Outline each blood parasite and name the species.
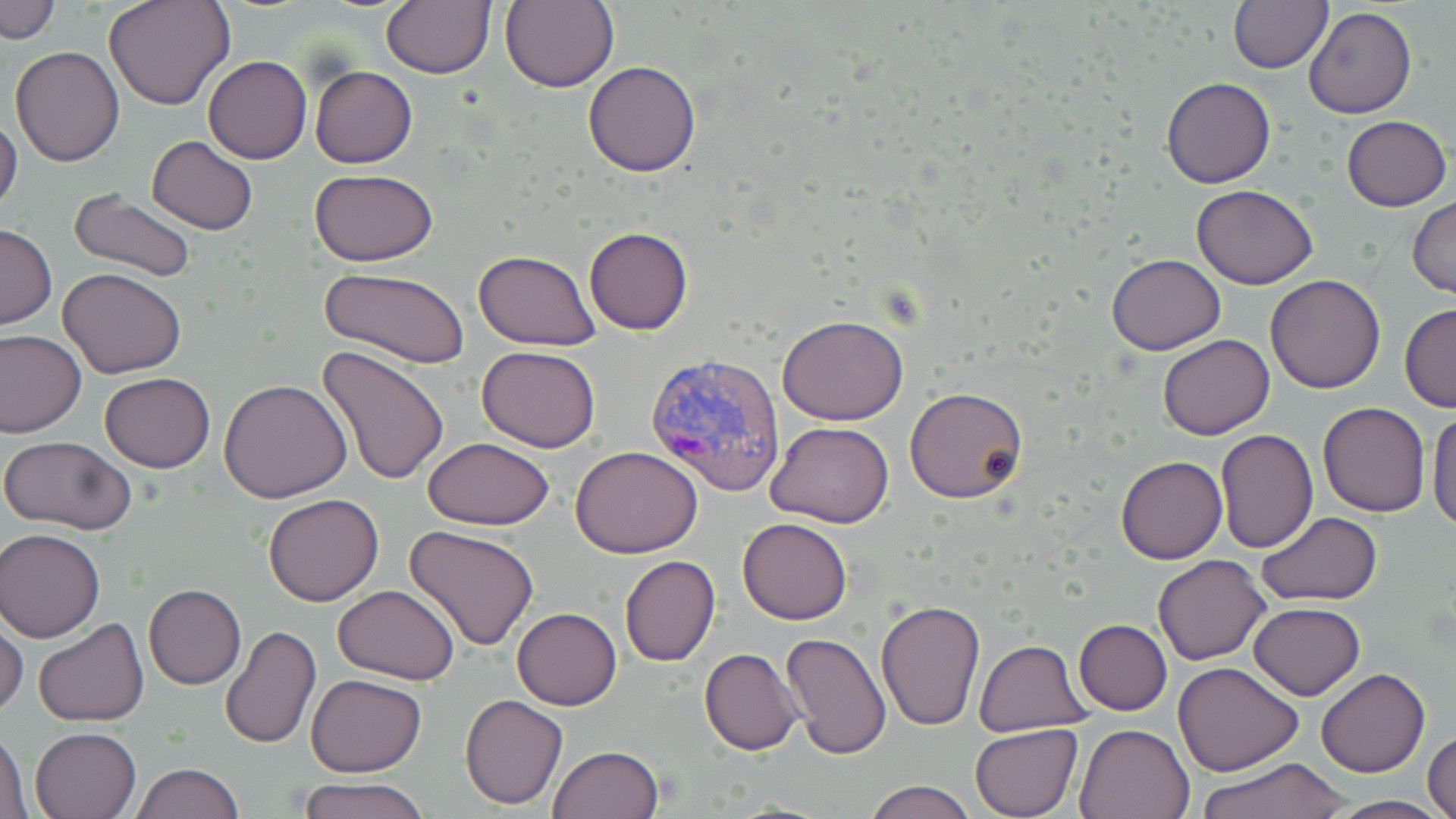

Approximate bounding boxes as (x1,y1)-(x2,y2) corner pairs in pixels.
Plasmodium vivax-infected red blood cells: (642,351)-(788,497).
No Plasmodium falciparum, Plasmodium ovale, Plasmodium malariae, Babesia divergens, or Trypanosoma brucei observed.

Uninfected red blood cell locations: (2,0)-(62,44), (103,0)-(235,111), (381,0)-(495,79), (1228,0)-(1334,74), (499,1)-(618,93), (1302,7)-(1417,118), (10,46)-(126,166), (204,57)-(312,164), (583,61)-(700,176), (309,65)-(417,167), (1159,76)-(1276,188), (1340,114)-(1451,211), (0,115)-(22,220), (147,136)-(260,235), (309,169)-(438,267), (1192,185)-(1319,289), (67,188)-(198,283), (1409,197)-(1456,297), (0,223)-(57,329), (584,226)-(693,336), (472,249)-(598,348), (1105,254)-(1228,355), (58,267)-(187,380), (320,267)-(471,369), (1265,274)-(1386,394), (1399,304)-(1456,413), (778,315)-(908,423), (0,329)-(85,438), (1156,334)-(1275,439), (316,345)-(448,485), (476,345)-(601,452), (99,372)-(216,472), (219,379)-(351,503), (904,388)-(1028,503), (1318,401)-(1430,518), (1427,407)-(1456,531), (765,421)-(894,529), (1214,429)-(1317,552), (0,436)-(136,533), (424,436)-(554,529), (571,445)-(703,559), (1116,455)-(1227,564), (262,494)-(383,607), (1258,512)-(1383,605), (738,517)-(853,625), (405,523)-(541,650), (1,529)-(105,642), (1152,554)-(1271,665), (619,555)-(720,667), (144,584)-(246,689), (332,584)-(460,683), (876,599)-(986,731), (1247,601)-(1365,700), (512,608)-(622,710), (0,615)-(28,717), (32,617)-(149,727), (1074,620)-(1172,715), (218,626)-(321,750), (780,630)-(891,759), (972,638)-(1092,735), (699,648)-(805,755), (1172,661)-(1302,777), (1317,668)-(1430,778), (306,673)-(426,777), (460,693)-(568,809), (1076,721)-(1197,818), (969,723)-(1082,817), (0,724)-(32,819), (30,725)-(143,819), (1424,730)-(1456,819), (547,745)-(664,819), (1196,757)-(1352,818), (130,763)-(244,818), (297,778)-(431,819), (863,779)-(980,819), (1328,795)-(1448,818). Slide-level diagnosis: Plasmodium vivax. Single field of view. 1000x magnification. Image is 1456×819 pixels. May-Grünwald-Giemsa stain. Light microscopy. Thin blood smear.